Name the parasite shown.
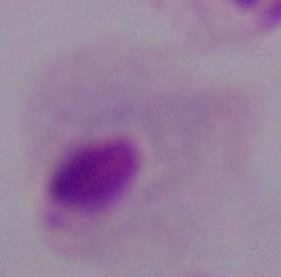
A trichomonad.

modality: micrograph
magnification: 1000x